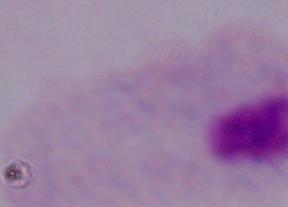

modality = photomicrograph
identification = trichomonad
magnification = 1000x